Locate and identify every blood parasite.
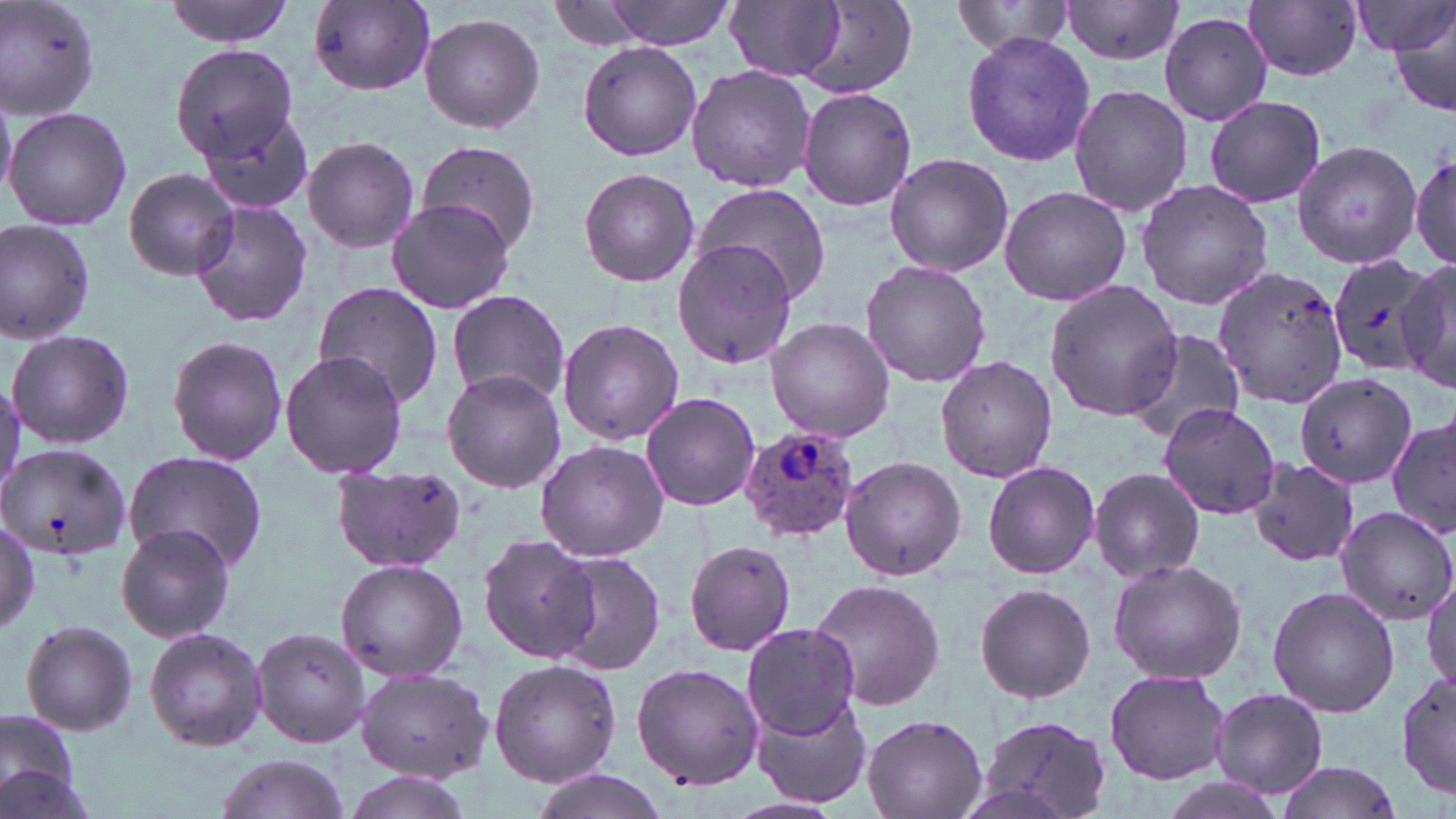

Approximate bounding boxes as (x1,y1)-(x2,y2) corner pairs in pixels.
Plasmodium ovale-infected red blood cells: (739,428)-(857,541).
No Plasmodium falciparum, Plasmodium malariae, Plasmodium vivax, Babesia divergens, or Trypanosoma brucei observed.

slide-level diagnosis = Plasmodium ovale
modality = light microscopy
magnification = 1000x
image size = 1456×819 pixels
uninfected red blood cell locations = approximate bounding boxes as (x1,y1)-(x2,y2) corner pairs in pixels: (0,0)-(99,122), (164,0)-(296,46), (600,0)-(738,51), (949,0)-(1077,59), (1357,0)-(1452,65), (726,1)-(846,82), (1061,1)-(1187,67), (307,2)-(437,96), (1244,2)-(1363,81), (799,4)-(919,98), (1387,6)-(1456,120), (1158,10)-(1274,127), (419,11)-(546,134), (961,30)-(1097,168), (1168,33)-(1296,186), (170,40)-(300,164), (577,42)-(702,162), (686,64)-(815,194), (0,84)-(17,203), (1067,85)-(1193,217), (797,87)-(917,211), (1203,95)-(1327,208), (5,104)-(132,231), (198,110)-(314,216), (302,134)-(421,253), (1290,139)-(1423,270), (415,140)-(544,254), (1409,143)-(1456,274), (884,154)-(1014,278), (124,167)-(238,281), (578,169)-(699,287), (1135,179)-(1276,311), (692,183)-(832,307), (998,186)-(1133,307), (386,199)-(514,314), (190,201)-(315,329), (0,218)-(97,346), (674,239)-(799,367), (1324,250)-(1439,377), (861,260)-(991,389), (1394,260)-(1456,394), (1212,266)-(1351,410), (1045,279)-(1181,423), (312,282)-(445,410), (445,290)-(572,405), (557,318)-(684,444), (765,318)-(895,443), (6,327)-(135,449), (1126,328)-(1249,444), (165,335)-(289,466), (279,350)-(408,479), (935,356)-(1057,481), (441,368)-(567,492), (1294,372)-(1418,490), (640,392)-(762,511), (1157,401)-(1281,520), (1386,414)-(1456,541), (536,440)-(667,562), (0,441)-(132,565), (122,450)-(268,575), (840,457)-(965,581), (1244,459)-(1360,565), (986,461)-(1101,578), (329,465)-(463,577), (1089,466)-(1206,585), (1334,504)-(1456,626), (0,517)-(40,636), (115,523)-(234,643), (476,533)-(599,664), (685,542)-(798,656), (546,551)-(666,679), (1107,557)-(1247,683), (334,558)-(468,681), (1422,572)-(1455,700), (808,577)-(947,712), (973,583)-(1096,703), (1267,585)-(1400,719), (19,620)-(138,735), (741,623)-(861,739), (144,625)-(268,753), (252,627)-(371,749), (488,661)-(621,788), (632,663)-(765,790), (355,666)-(493,781), (1398,669)-(1456,798), (1105,670)-(1230,784), (1209,688)-(1329,799), (751,692)-(871,809), (0,709)-(81,803), (861,712)-(988,819), (976,716)-(1112,819), (211,754)-(352,819), (1273,759)-(1401,819), (0,762)-(98,819), (528,770)-(668,819), (343,773)-(478,819)
preparation = thin blood film
field of view = single
stain = May-Grünwald-Giemsa